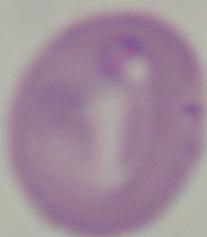

Summary:
  - Magnification: 1000x
  - Identification: Babesia
  - Modality: micrograph